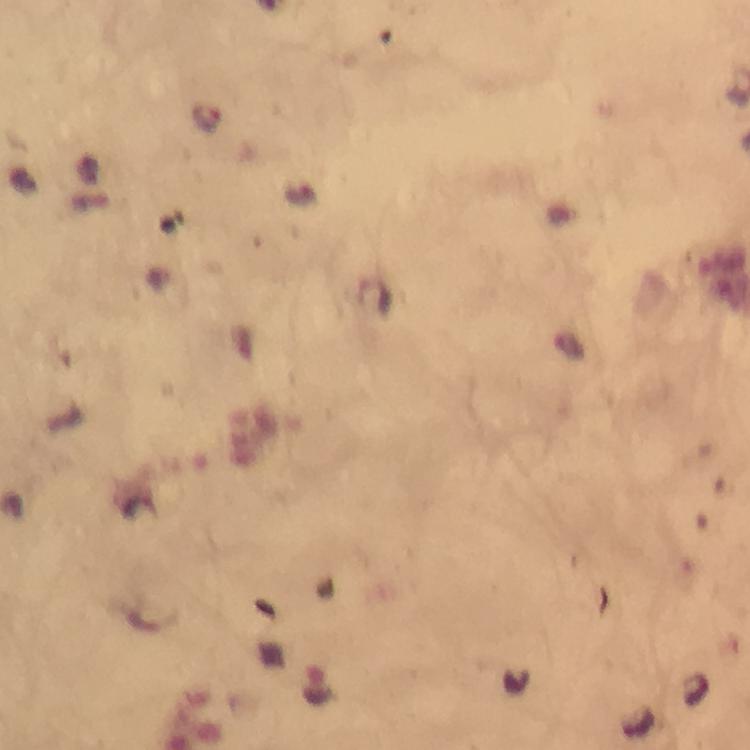 Approximate centers as {x, y} in pixels. Malaria parasite locations: {209, 119}. Smartphone photograph taken through a microscope. At 100x magnification. Immersion oil applied. A crop from one field of view. Giemsa stain. From a malaria diagnostic workup. Thick blood film. Image is 750×750 pixels.